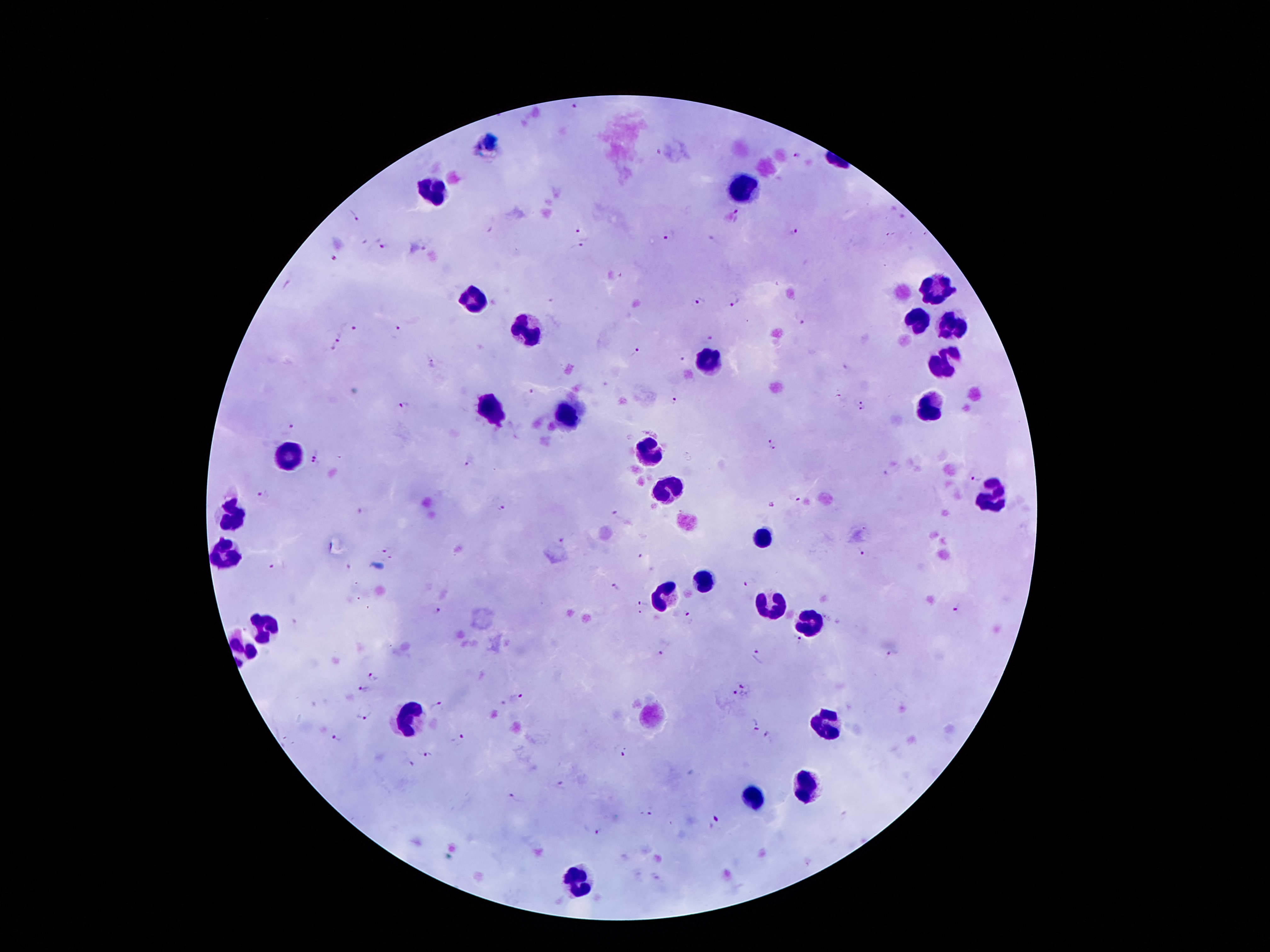

Approximate centers as {x, y} in pixels.
Summary:
  - Plasmodium parasite locations: {574, 108}, {796, 156}, {353, 216}, {740, 216}, {587, 230}, {794, 235}, {669, 236}, {384, 244}, {427, 245}, {576, 248}, {335, 256}, {553, 299}, {735, 301}, {699, 302}, {803, 318}, {357, 328}, {398, 333}, {340, 337}, {710, 337}, {334, 352}, {636, 352}, {682, 357}, {435, 363}, {530, 396}, {837, 396}, {858, 400}, {675, 401}, {403, 407}, {862, 411}, {288, 427}, {770, 436}, {774, 449}, {318, 453}, {315, 465}, {469, 465}, {891, 472}, {973, 477}, {263, 496}, {797, 498}, {771, 504}, {501, 507}, {619, 514}, {563, 539}, {383, 551}, {861, 551}, {641, 555}, {394, 556}, {273, 566}, {749, 583}, {615, 587}, {641, 603}, {957, 609}, {437, 610}, {687, 614}, {642, 616}, {798, 640}, {890, 654}, {659, 655}, {759, 655}, {375, 676}, {744, 687}, {364, 689}, {733, 694}, {517, 698}, {437, 706}, {364, 715}, {754, 727}, {769, 736}, {337, 739}, {461, 741}, {623, 752}, {427, 755}, {410, 764}, {561, 788}, {514, 799}, {650, 810}, {718, 821}, {599, 832}
  - Leukocyte locations: {737, 187}, {435, 188}, {935, 290}, {475, 302}, {915, 321}, {947, 329}, {529, 331}, {945, 360}, {705, 364}, {491, 410}, {927, 410}, {567, 414}, {649, 452}, {291, 462}, {665, 488}, {991, 496}, {235, 520}, {761, 536}, {223, 556}, {703, 582}, {661, 596}, {769, 602}, {805, 624}, {265, 626}, {407, 720}, {825, 722}, {807, 788}, {753, 796}, {577, 878}
  - Patient malaria status: positive for Plasmodium falciparum
  - Preparation: thick blood film
  - Stain: Giemsa
  - Field of view: single
  - Capture: smartphone through the microscope eyepiece
  - Magnification: 100x
  - Image size: 1270×952 pixels